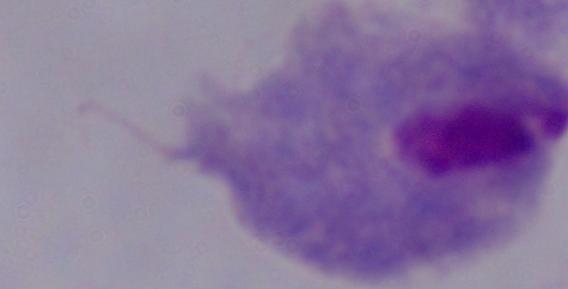 Captured at 1000x magnification. Photomicrograph. A trichomonad is seen.